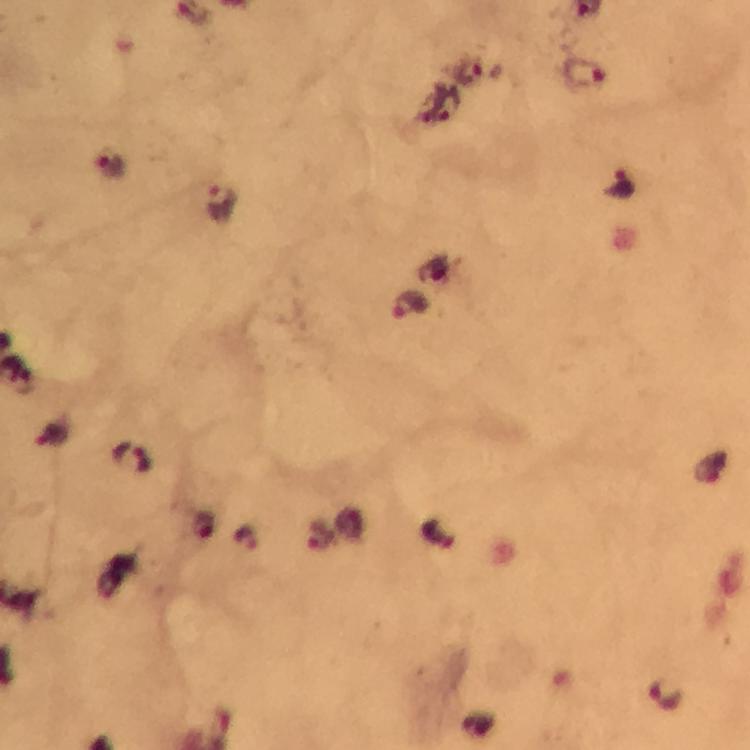
malaria parasite locations = approximate centers as [x, y] in pixels: [472, 71], [584, 75], [445, 105], [111, 165], [621, 186], [224, 205], [411, 304], [52, 435], [133, 459], [322, 538], [247, 539], [666, 695]
capture = smartphone camera through the microscope
context = from a diagnostic examination for malaria
preparation = thick blood film
cropped from = one field of view
image size = 750×750 pixels
immersion oil = applied
magnification = 100x
stain = Giemsa